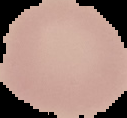
Segmented cell region on a black background. From a thin blood film. Image is 127×118 pixels. Malaria status: uninfected.